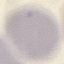

malaria status = uninfected
capture = smartphone through the microscope eyepiece
preparation = thin blood film
image type = cell patch, automatically extracted from a larger field of view and resized to 64 × 64 pixels
stain = Giemsa